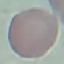

malaria status = uninfected
image type = automatically extracted cell patch, resized to 64 × 64 pixels
stain = Giemsa
preparation = thin smear
capture = smartphone through the microscope eyepiece